Report the malaria status of this cell.
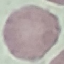
It is uninfected.

{
  "preparation": "thin blood film",
  "stain": "Giemsa",
  "capture": "smartphone camera at the microscope eyepiece",
  "image_type": "automatically extracted cell patch, resized to 64 × 64 pixels"
}